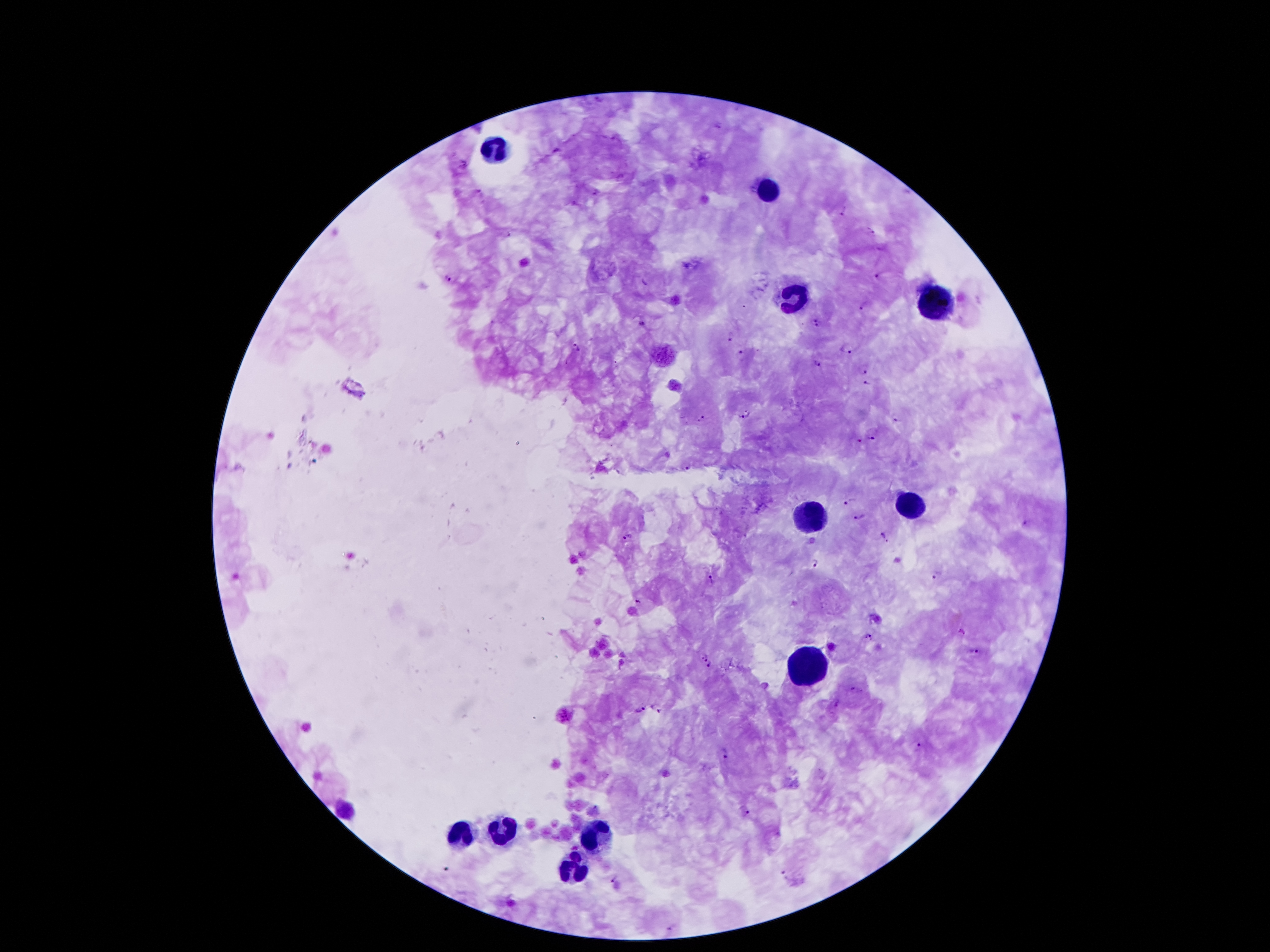

magnification: 100x
capture: smartphone camera through the microscope eyepiece
leukocyte_locations: 'approximate centers as [x, y] in pixels: [494, 153], [769, 189], [794, 298], [935, 303], [910, 505], [810, 518], [803, 671], [497, 830], [458, 834], [594, 834], [576, 868]'
field_of_view: one from this slide
image_size: 1270×952 pixels
malaria_parasite_locations: 'approximate centers as [x, y] in pixels: [465, 165], [478, 191], [842, 210], [871, 232], [879, 276], [449, 278], [643, 282], [863, 307], [641, 323], [815, 324], [731, 336], [846, 349], [574, 350], [742, 353], [818, 363], [864, 371], [867, 385], [745, 417], [701, 419], [896, 420], [872, 435], [857, 442], [686, 467], [852, 501], [861, 517], [882, 535], [628, 536], [817, 563], [937, 576], [712, 579], [637, 602], [867, 638], [973, 651], [705, 656], [709, 664], [856, 688], [659, 707], [639, 709], [919, 747], [727, 754], [745, 809], [785, 873], [613, 879], [671, 928]'
stain: Giemsa
preparation: thick peripheral-blood smear
patient_malaria_status: infected with Plasmodium falciparum